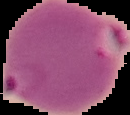
{
  "preparation": "thin blood film",
  "image_type": "segmented cell region with the area outside set to black",
  "result": "Plasmodium parasites detected",
  "image_size": "130×115 pixels"
}